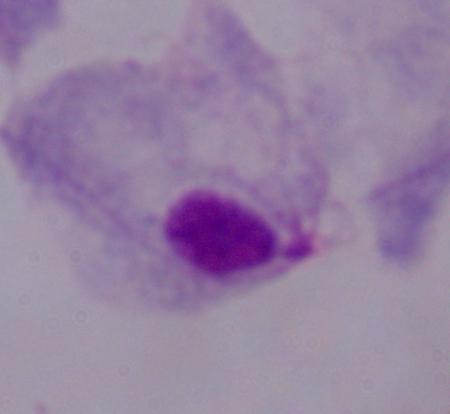
identification: trichomonad
modality: photomicrograph
magnification: 1000x